Classify this cell by malaria status.
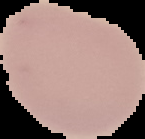

It is uninfected.

preparation = thin blood smear
image type = segmented cell region with the area outside set to black
image size = 145×139 pixels